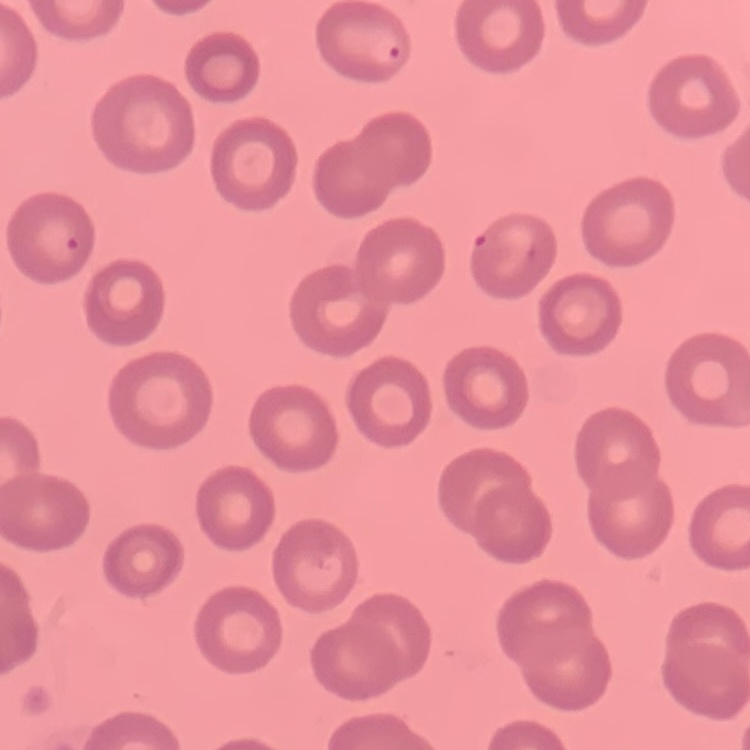
The erythrocytes exhibit no rouleaux formation. Square crop of a larger photomicrograph. Thin blood smear. Field's or Giemsa stain.